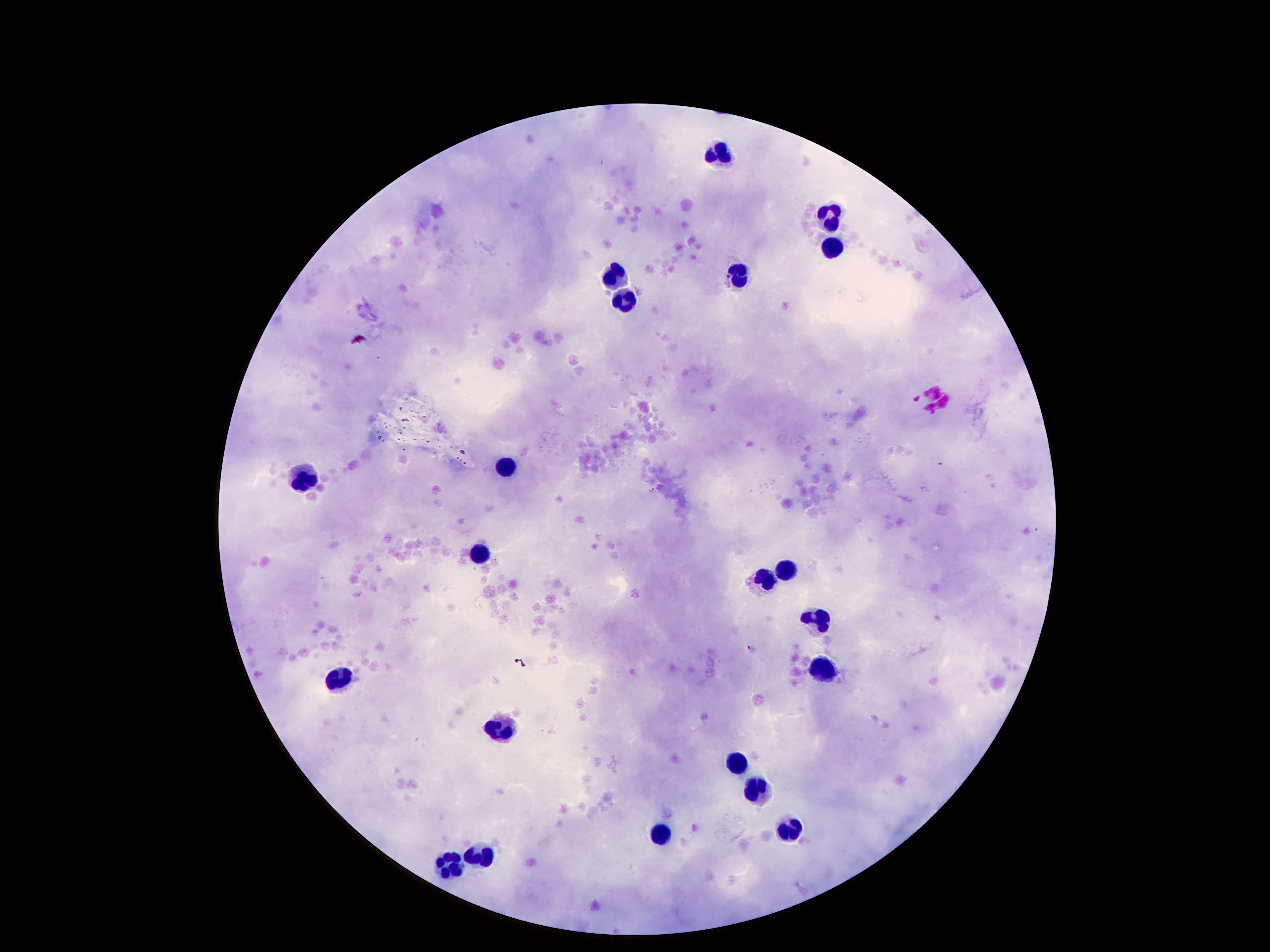
Approximate centers as (x, y) in pixels.
Summary:
  - Leukocyte locations: (726, 155), (837, 211), (833, 252), (617, 270), (740, 273), (626, 302), (504, 466), (306, 475), (477, 556), (792, 570), (769, 581), (822, 620), (822, 674), (338, 677), (499, 729), (737, 761), (756, 790), (787, 824), (663, 834), (483, 854), (451, 870)
  - Field of view: single
  - Preparation: thick peripheral-blood smear
  - Stain: Giemsa
  - Patient malaria status: negative
  - Capture: smartphone camera through the microscope eyepiece
  - Image size: 1270×952 pixels
  - Magnification: 100x